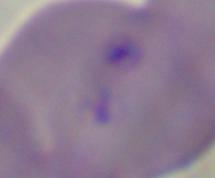

Summary:
  - Magnification: 1000x
  - Modality: micrograph
  - Identification: Babesia